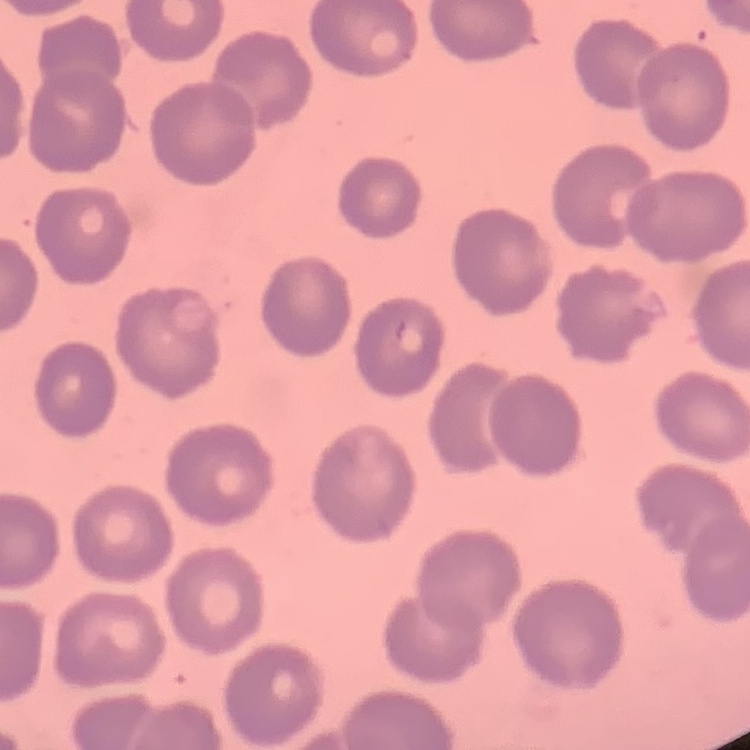
red_blood_cell_morphology: no rouleaux formation
image_type: one tile cut from a larger photomicrograph
stain: Field's or Giemsa
preparation: thin blood film